Assess the morphology of the erythrocytes.
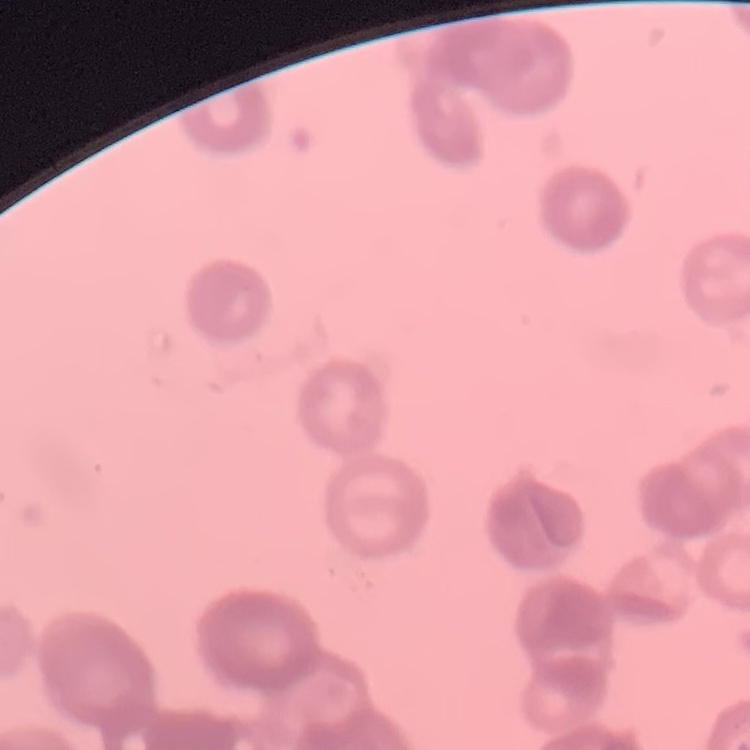
They show rouleaux formation.

Summary:
  - Image type: square crop of a larger photomicrograph
  - Stain: Field's or Giemsa
  - Preparation: thin blood film